Assess the morphology of the red blood cells.
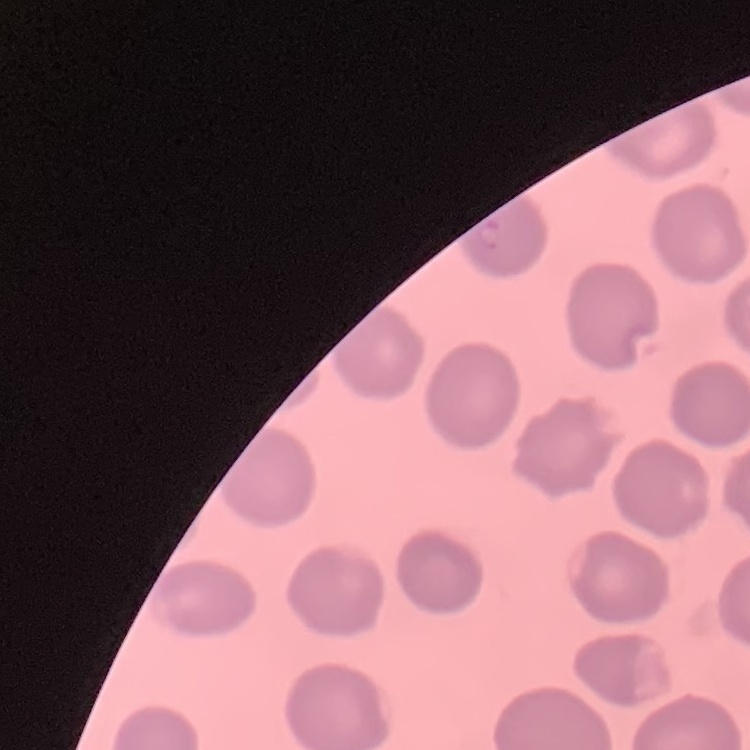
No rouleaux formation.

stain: Field's or Giemsa
image_type: square crop of a larger photomicrograph
preparation: thin blood smear